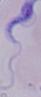
{
  "identification": "trypanosome",
  "magnification": "1000x",
  "modality": "micrograph"
}